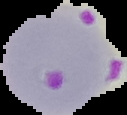

Summary:
  - Malaria status: parasitized
  - Preparation: thin blood film
  - Image size: 127×115 pixels
  - Image type: segmented cell region on a black background